State which parasite is depicted.
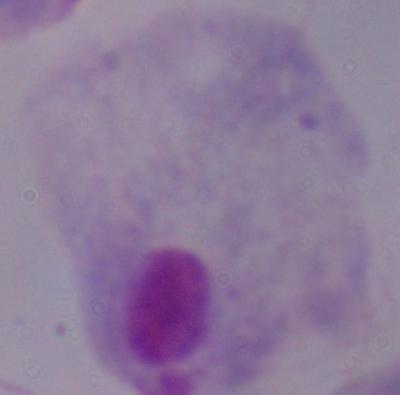
This is a trichomonad.

Photomicrograph. 1000x magnification.